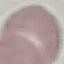
Summary:
  - Malaria status: uninfected
  - Image type: automatically extracted cell patch, resized to 64 × 64 pixels
  - Stain: Giemsa
  - Capture: smartphone camera at the microscope eyepiece
  - Preparation: thin blood film